Locate every blood parasite and identify its species.
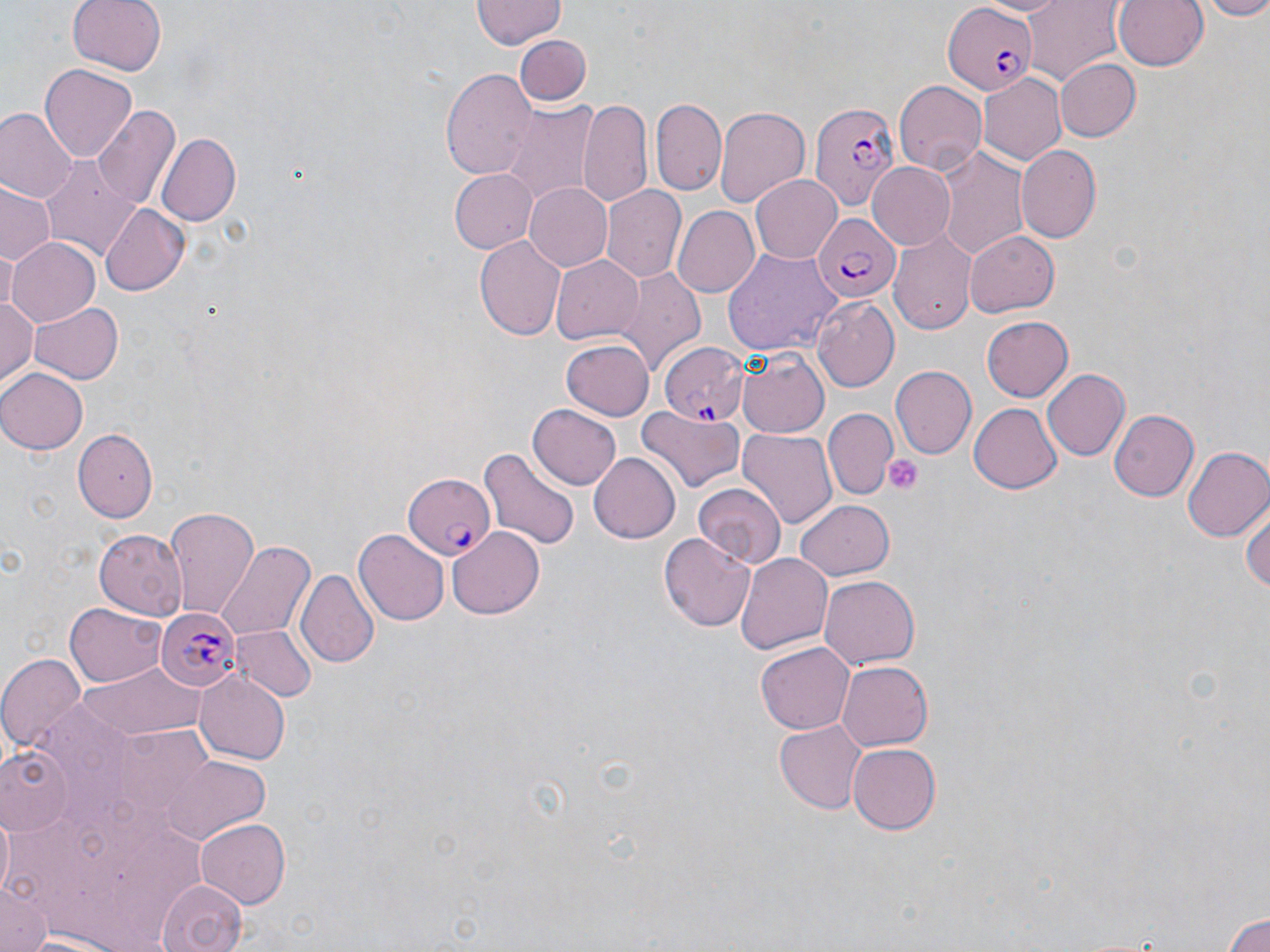
Approximate bounding boxes as (x1, y1, x2, y2) in pixels.
Plasmodium falciparum-infected red blood cells: (944, 0, 1038, 96), (808, 99, 898, 211), (810, 212, 898, 302), (660, 341, 749, 424), (403, 471, 497, 560), (155, 606, 241, 690).
No Plasmodium ovale, Plasmodium malariae, Plasmodium vivax, Babesia divergens, or Trypanosoma brucei observed.

Summary:
  - Platelet locations: (884, 455, 923, 496)
  - Uninfected red blood cell locations: (68, 0, 166, 77), (471, 0, 565, 50), (973, 0, 1073, 18), (1021, 0, 1123, 85), (1113, 0, 1210, 72), (1190, 0, 1270, 19), (513, 36, 591, 106), (1056, 58, 1142, 142), (40, 63, 135, 160), (442, 69, 537, 183), (979, 72, 1067, 165), (895, 79, 987, 174), (652, 97, 728, 197), (579, 100, 653, 208), (498, 103, 598, 202), (92, 105, 180, 210), (714, 105, 809, 209), (0, 108, 77, 205), (156, 133, 240, 226), (935, 145, 1029, 259), (1016, 145, 1101, 243), (39, 156, 142, 264), (866, 161, 956, 249), (449, 168, 535, 253), (751, 174, 844, 263), (523, 182, 612, 270), (1, 185, 56, 267), (601, 186, 685, 283), (98, 202, 190, 297), (673, 205, 759, 297), (964, 230, 1059, 317), (889, 231, 974, 337), (475, 236, 567, 341), (7, 237, 100, 328), (725, 247, 845, 357), (550, 253, 643, 345), (613, 268, 706, 373), (0, 293, 39, 389), (812, 297, 900, 393), (27, 300, 121, 384), (980, 317, 1072, 402), (561, 339, 653, 422), (735, 349, 829, 440), (891, 367, 976, 459), (0, 368, 86, 454), (1043, 369, 1130, 461), (969, 403, 1062, 494), (528, 405, 623, 488), (637, 405, 744, 496), (826, 409, 898, 498), (1108, 409, 1198, 503), (738, 428, 836, 527), (74, 431, 159, 521), (479, 446, 581, 553), (1183, 446, 1270, 540), (589, 450, 684, 542), (693, 481, 785, 567), (1243, 495, 1270, 599), (796, 498, 895, 579), (165, 507, 258, 618), (447, 526, 547, 620), (95, 529, 187, 618), (355, 530, 449, 625), (659, 531, 755, 634), (214, 540, 314, 644), (736, 551, 834, 655), (298, 567, 379, 667), (819, 574, 919, 669), (67, 602, 167, 686), (231, 625, 317, 704), (756, 642, 854, 733), (0, 654, 86, 760), (79, 659, 206, 743), (836, 660, 932, 750), (195, 673, 289, 763), (773, 719, 868, 813), (848, 742, 940, 834), (2, 745, 74, 833), (160, 755, 270, 846), (2, 812, 17, 902), (197, 818, 291, 909), (157, 878, 246, 952), (1, 883, 50, 952), (1223, 908, 1270, 952), (17, 930, 132, 951)
  - Slide-level diagnosis: Plasmodium falciparum
  - Modality: light microscopy
  - Field of view: single
  - Stain: May-Grünwald-Giemsa
  - Image size: 1270×952 pixels
  - Preparation: thin blood smear
  - Magnification: 1000x